Locate platelets.
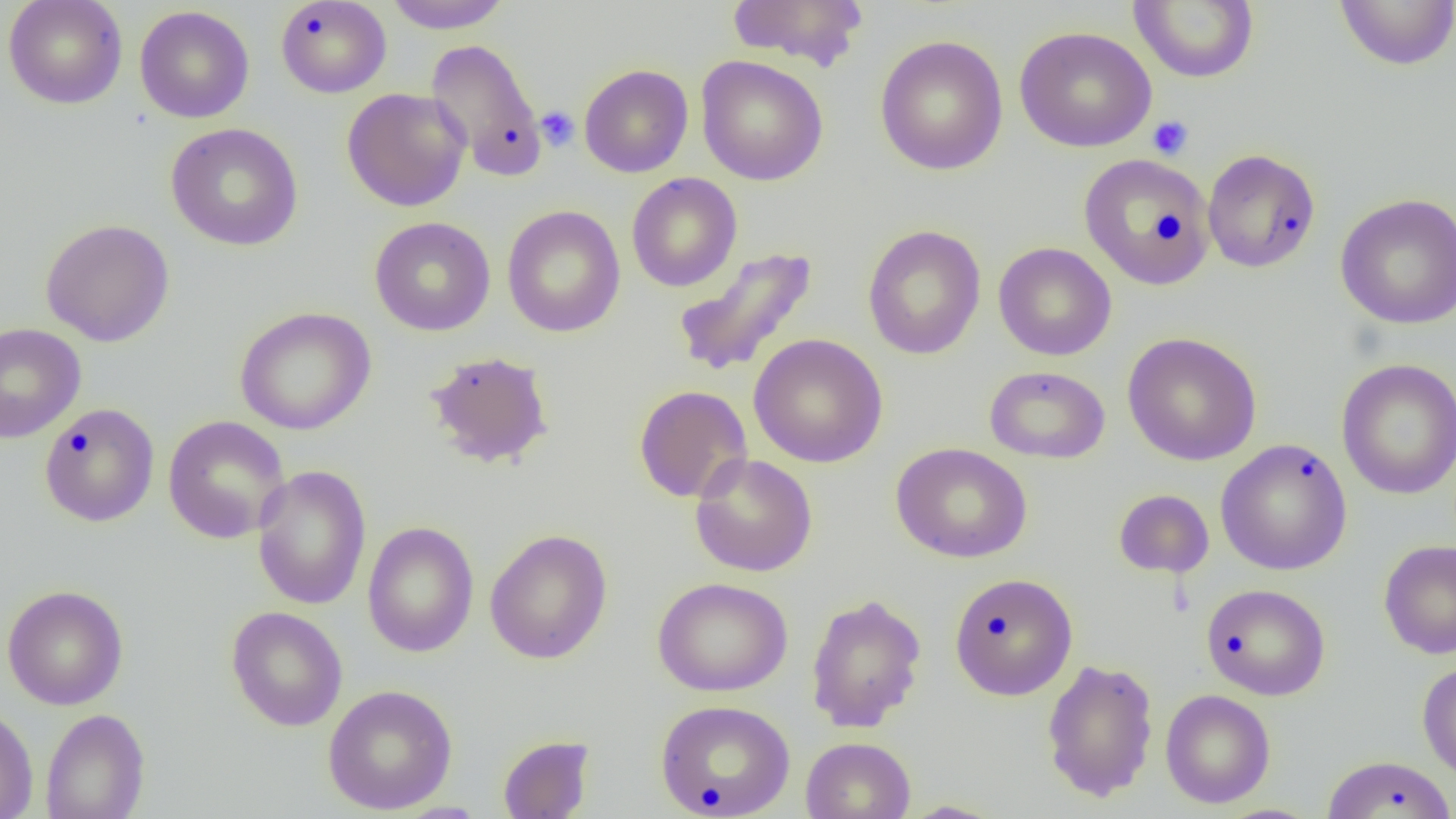
Approximate bounding boxes as [x1, y1, x2, y2] in pixels.
Platelets: [535, 105, 580, 152], [1147, 115, 1194, 160], [1151, 207, 1186, 245].

Uninfected red blood cell locations: [3, 0, 128, 109], [383, 0, 513, 33], [725, 0, 871, 71], [1128, 0, 1260, 84], [1334, 0, 1456, 70], [275, 1, 392, 98], [134, 5, 254, 123], [1014, 26, 1157, 153], [874, 34, 1009, 175], [424, 38, 546, 181], [696, 55, 828, 186], [578, 63, 694, 178], [342, 87, 471, 212], [165, 122, 303, 251], [1202, 148, 1321, 273], [1078, 153, 1214, 289], [626, 173, 742, 293], [1336, 193, 1456, 329], [502, 205, 626, 338], [369, 216, 496, 336], [40, 218, 175, 346], [862, 224, 986, 360], [994, 242, 1117, 360], [672, 246, 818, 380], [235, 306, 376, 435], [0, 322, 86, 443], [1122, 332, 1262, 466], [748, 333, 888, 468], [424, 350, 554, 469], [1336, 357, 1456, 500], [984, 365, 1111, 464], [634, 385, 752, 503], [39, 403, 160, 527], [162, 415, 290, 543], [1215, 439, 1353, 576], [891, 442, 1032, 563], [690, 453, 818, 577], [251, 464, 372, 611], [1113, 489, 1214, 579], [362, 521, 479, 658], [484, 528, 613, 664], [1378, 539, 1456, 660], [949, 572, 1078, 700], [652, 577, 792, 697], [1201, 583, 1330, 701], [2, 584, 128, 710], [805, 592, 927, 732], [225, 606, 348, 731], [1041, 657, 1159, 802], [1416, 661, 1456, 781], [322, 684, 458, 815], [1160, 689, 1275, 808], [655, 699, 795, 818], [0, 705, 38, 819], [40, 708, 150, 819], [497, 734, 595, 818], [801, 736, 916, 819], [1322, 754, 1456, 819]. Slide-level diagnosis: no evidence of blood parasites. Light microscopy. Image is 1456×819 pixels. Single field of view. 1000x magnification. Thin blood film.